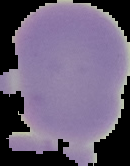

Malaria status: uninfected. The area outside the segmented cell region is set to black. From a thin blood smear. Image is 130×166 pixels.